Outline each Plasmodium ovale-infected red blood cell.
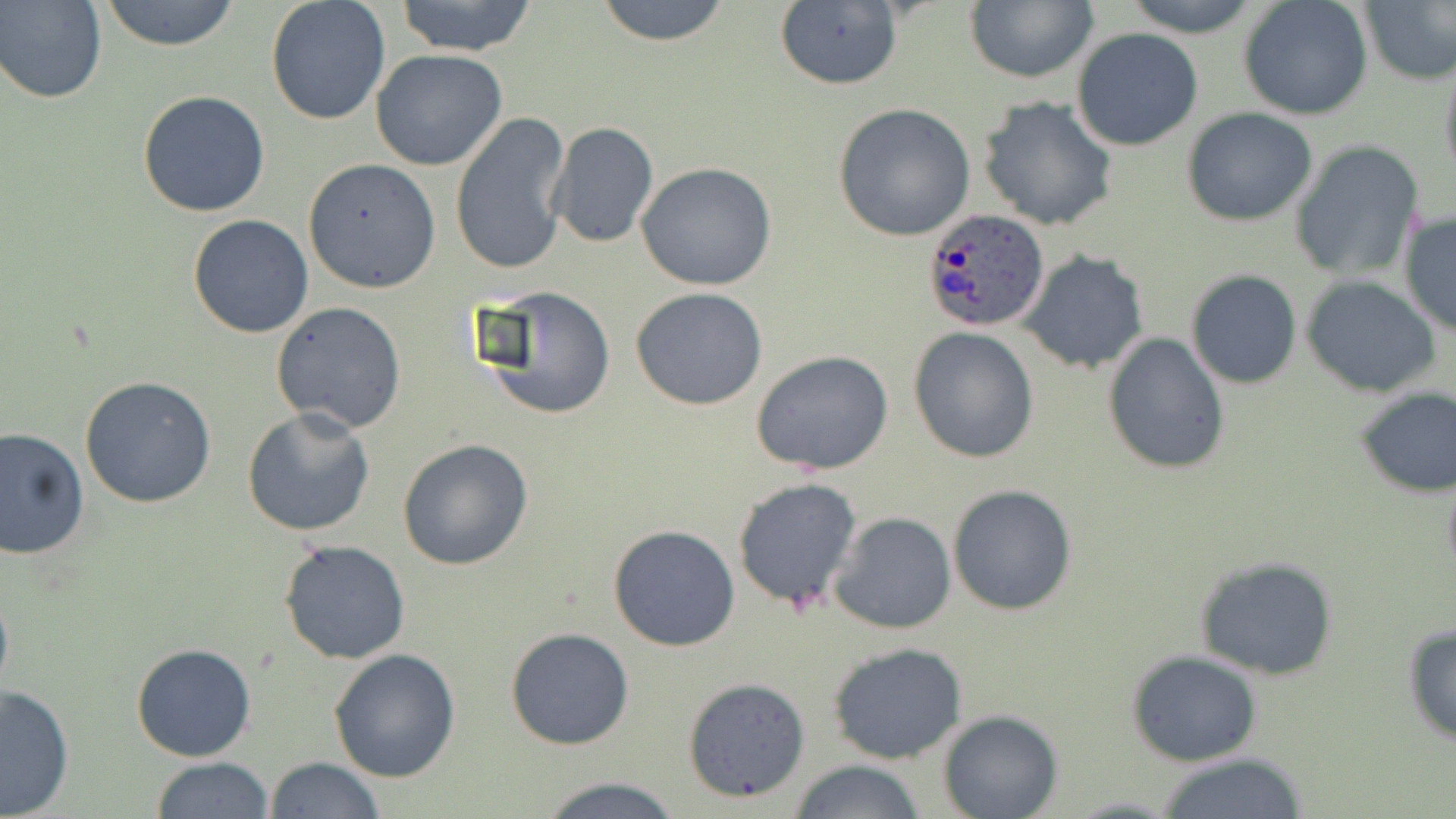
Approximate bounding boxes as (x1, y1, x2, y2) in pixels.
Plasmodium ovale-infected red blood cells: (922, 211, 1049, 334).

Summary:
  - Uninfected red blood cell locations: (1, 0, 106, 103), (97, 0, 243, 50), (391, 0, 540, 56), (593, 0, 734, 48), (1118, 0, 1267, 35), (1239, 0, 1373, 121), (1359, 0, 1455, 86), (265, 1, 391, 126), (773, 1, 903, 92), (965, 1, 1097, 83), (1071, 28, 1202, 150), (370, 49, 510, 172), (1438, 53, 1456, 184), (136, 90, 271, 217), (977, 95, 1118, 232), (833, 102, 976, 241), (1182, 109, 1317, 226), (450, 114, 572, 279), (546, 121, 660, 249), (1288, 141, 1426, 284), (302, 158, 441, 293), (636, 162, 777, 291), (1399, 212, 1456, 337), (187, 214, 314, 339), (1019, 251, 1149, 374), (1187, 271, 1302, 390), (1301, 274, 1442, 397), (473, 285, 618, 422), (628, 288, 770, 410), (272, 302, 407, 431), (908, 327, 1040, 464), (1103, 331, 1230, 474), (751, 350, 894, 475), (79, 375, 216, 508), (1354, 387, 1455, 496), (243, 406, 376, 537), (0, 428, 90, 561), (397, 439, 535, 571), (731, 477, 863, 614), (948, 484, 1077, 616), (830, 512, 956, 636), (608, 524, 741, 651), (279, 538, 411, 665), (1193, 557, 1339, 681), (0, 578, 13, 708), (1402, 622, 1456, 745), (504, 627, 634, 749), (826, 641, 969, 763), (130, 643, 257, 762), (329, 647, 461, 782), (1126, 651, 1263, 768), (683, 676, 812, 802), (0, 683, 75, 816), (939, 711, 1064, 819), (1153, 751, 1309, 819), (151, 756, 275, 817), (264, 756, 384, 818), (786, 759, 928, 819), (532, 774, 686, 817)
  - Slide-level diagnosis: Plasmodium ovale
  - Magnification: 1000x
  - Image size: 1456×819 pixels
  - Modality: light microscopy
  - Stain: May-Grünwald-Giemsa
  - Field of view: single
  - Preparation: thin blood film